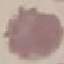

Summary:
  - Malaria status: uninfected
  - Preparation: thin blood film
  - Image type: cell patch, automatically extracted from a larger field of view and resized to 64 × 64 pixels
  - Stain: Giemsa
  - Capture: smartphone camera at the microscope eyepiece